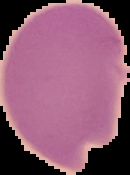

image size = 130×175 pixels
image type = cell region segmented out of the field of view; surrounding area masked to black
preparation = thin blood smear
malaria status = uninfected